Locate every blood parasite and identify its species.
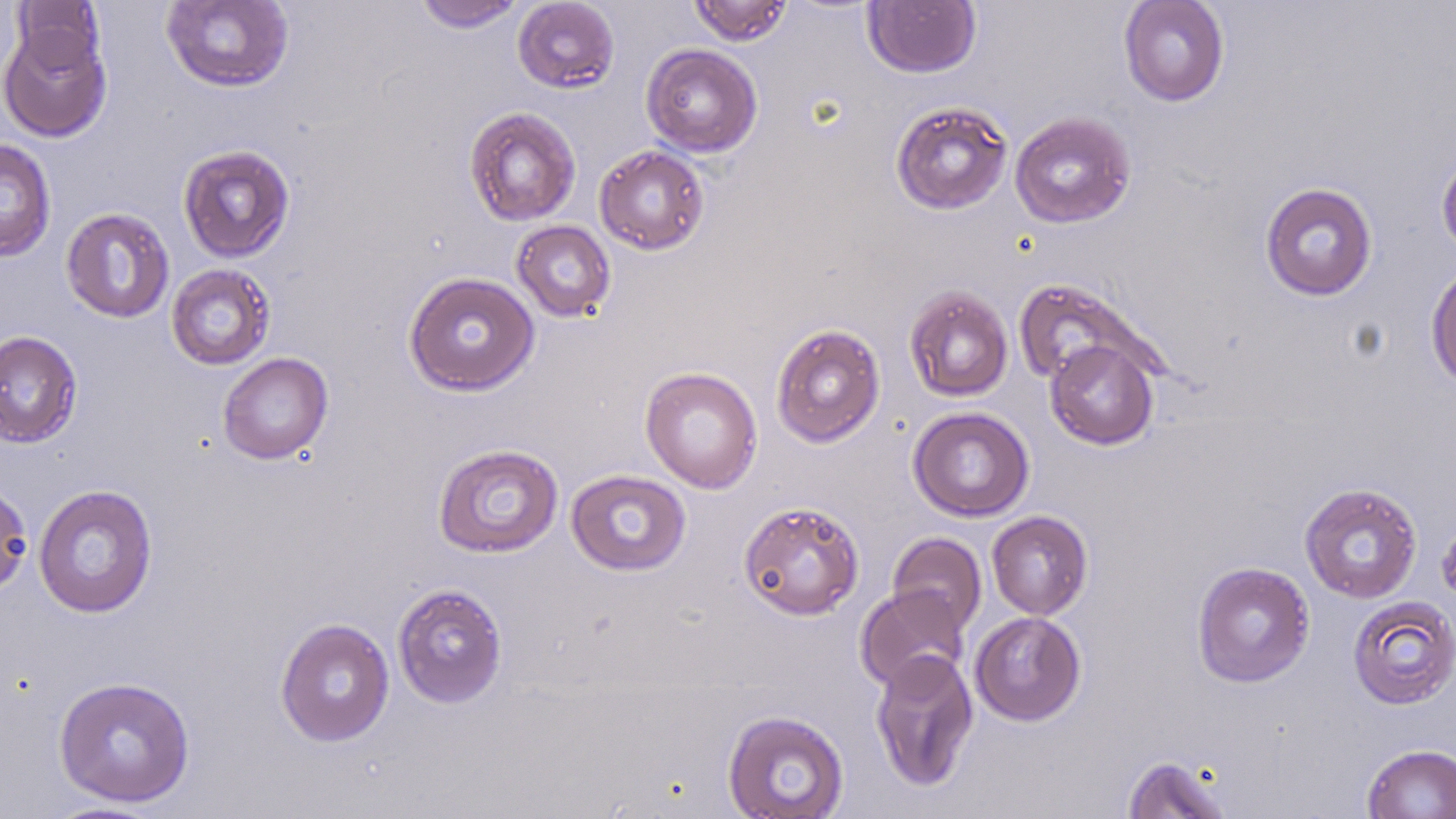
No blood parasites observed.

slide_level_diagnosis: no evidence of blood parasites
magnification: 1000x
preparation: thin blood film
field_of_view: single
uninfected_red_blood_cell_locations: 'approximate bounding boxes as [x1, y1, x2, y2] in pixels: [413, 0, 527, 33], [512, 0, 620, 94], [688, 0, 793, 46], [1118, 0, 1230, 107], [11, 1, 106, 77], [160, 1, 294, 92], [862, 1, 982, 78], [0, 23, 112, 143], [641, 43, 763, 157], [890, 100, 1013, 215], [463, 106, 581, 226], [1010, 111, 1136, 228], [0, 139, 57, 262], [177, 144, 295, 262], [594, 145, 710, 255], [1436, 149, 1456, 260], [1259, 181, 1378, 301], [60, 207, 175, 323], [511, 220, 616, 323], [1425, 261, 1456, 390], [166, 264, 276, 370], [403, 271, 540, 396], [1012, 279, 1146, 386], [904, 285, 1014, 403], [770, 322, 886, 448], [0, 330, 83, 448], [1045, 339, 1159, 450], [218, 352, 334, 465], [639, 366, 763, 493], [907, 406, 1035, 522], [432, 444, 564, 558], [566, 469, 692, 577], [0, 478, 33, 598], [1299, 482, 1422, 604], [32, 484, 158, 618], [738, 500, 865, 621], [986, 510, 1094, 620], [1437, 511, 1456, 610], [887, 532, 987, 636], [1191, 561, 1315, 688], [392, 583, 509, 709], [855, 585, 970, 693], [1347, 595, 1456, 709], [969, 611, 1087, 726], [274, 617, 395, 747], [870, 649, 979, 792], [53, 676, 196, 807], [722, 709, 850, 818], [1361, 743, 1456, 819], [1121, 754, 1236, 818], [39, 800, 169, 818]'
image_size: 1456×819 pixels
stain: May-Grünwald-Giemsa
modality: optical microscopy